Report the malaria status of this cell.
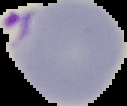

It is parasitized.

From a thin blood film. Cell region segmented out of the field of view; the surrounding area is masked to black. Image is 127×106 pixels.